Identify the parasite.
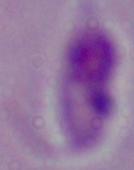

This is Leishmania.

Summary:
  - Magnification: 1000x
  - Modality: photomicrograph